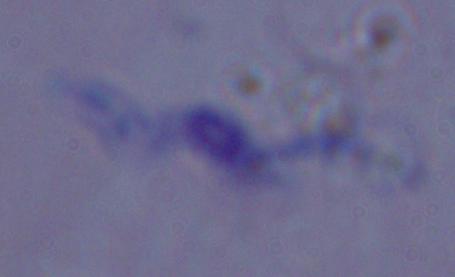
magnification: 1000x
identification: trypanosome
modality: photomicrograph